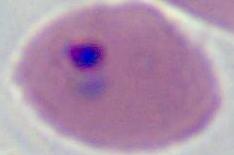

Summary:
  - Identification: Plasmodium
  - Modality: micrograph
  - Magnification: 400x or 1000x